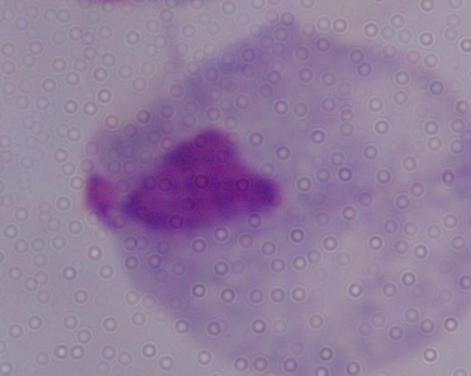
Micrograph. 1000x magnification. A trichomonad is shown.